Assess the morphology of the erythrocytes.
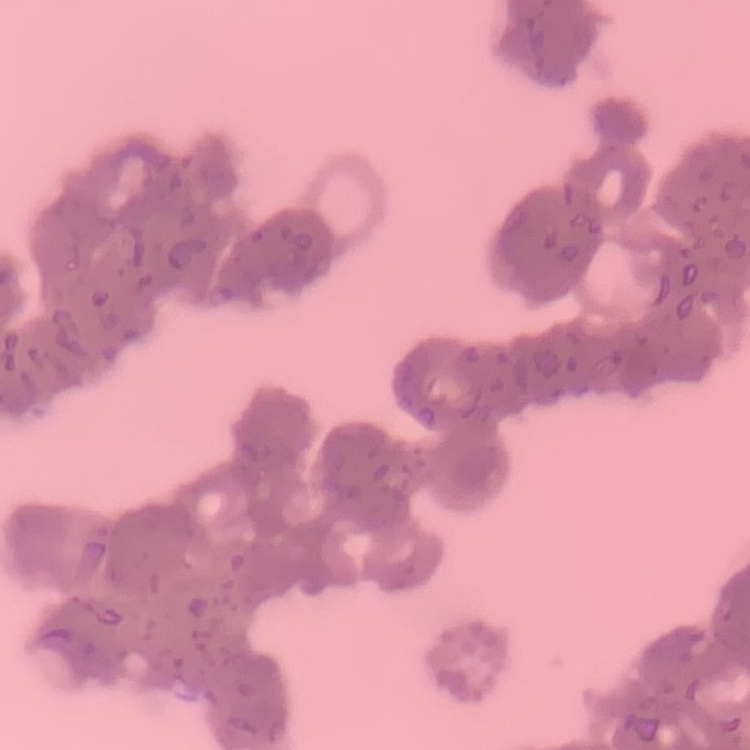
Rouleaux formation.

Summary:
  - Stain: Field's or Giemsa
  - Preparation: thin peripheral smear
  - Image type: one tile cut from a larger photomicrograph